Give the position of every malaria parasite.
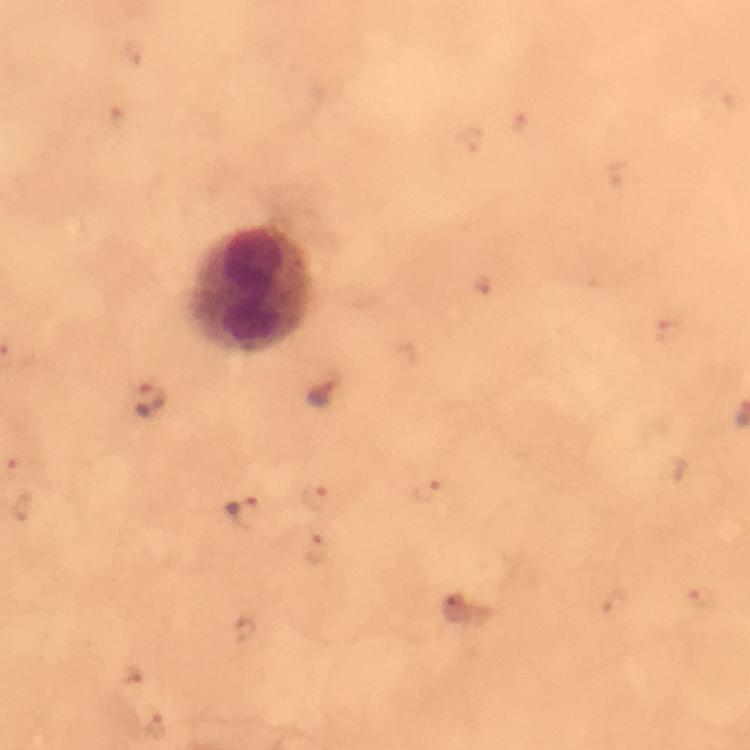

Approximate centers as {x, y} in pixels.
Malaria parasites: {320, 391}, {150, 400}, {245, 509}.

Leukocyte locations: {254, 288}. 100x magnification. From a malaria diagnostic workup. Thick blood film. Cropped region of a single field of view. Image is 750×750 pixels. Giemsa-stained preparation. Photographed through the microscope with a smartphone camera. Immersion oil was used.